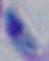

magnification: 1000x
modality: photomicrograph
identification: Toxoplasma gondii